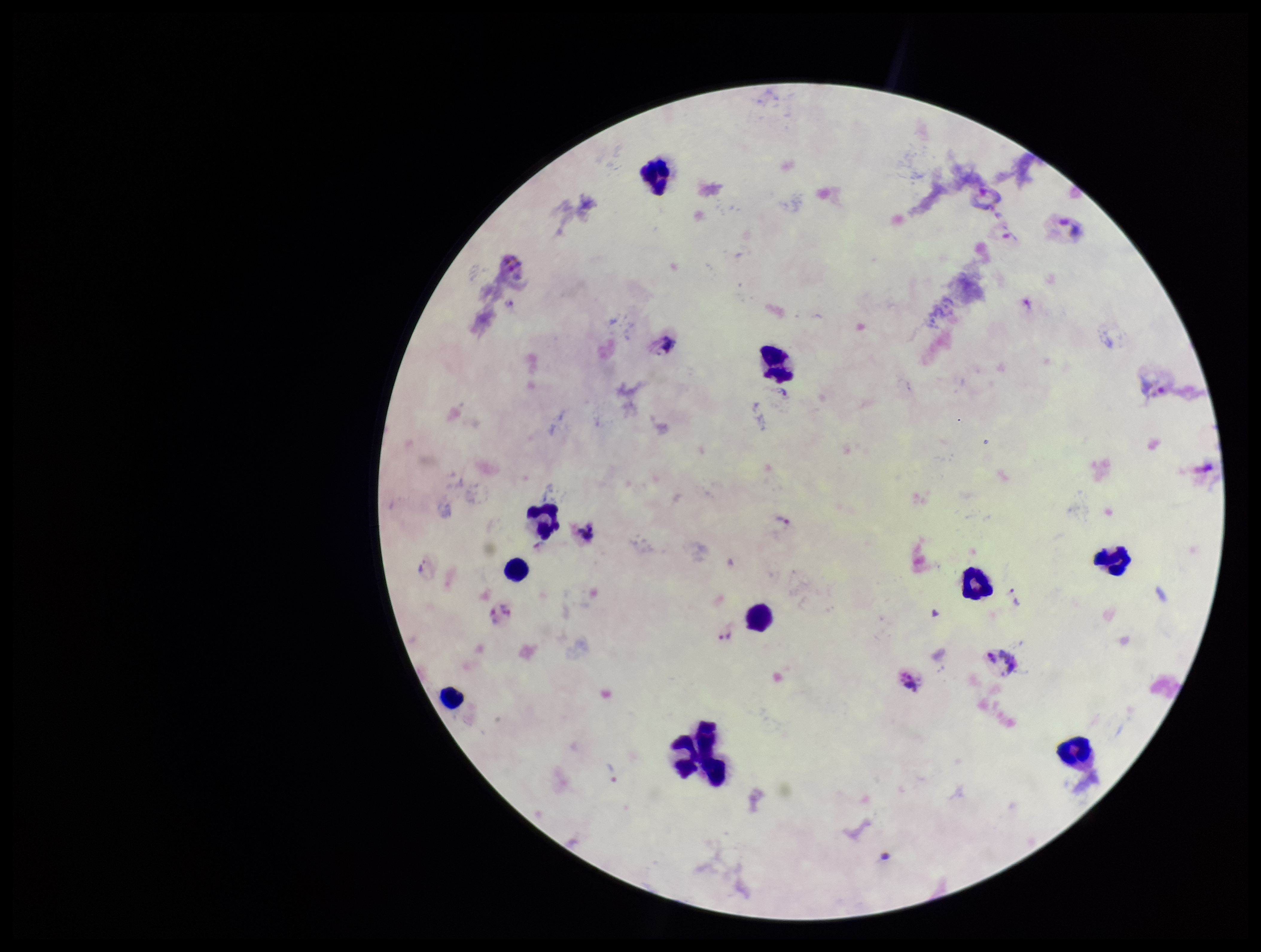 Giemsa stain. Single field of view. Species reported for this patient: Plasmodium vivax. Image is 1261×952 pixels. Leukocyte count: 11. Photographed through the microscope eyepiece with a smartphone camera. Preparation: thick blood smear. Patient malaria status: positive. Plasmodium parasites: none detected. Parasite count: 0.